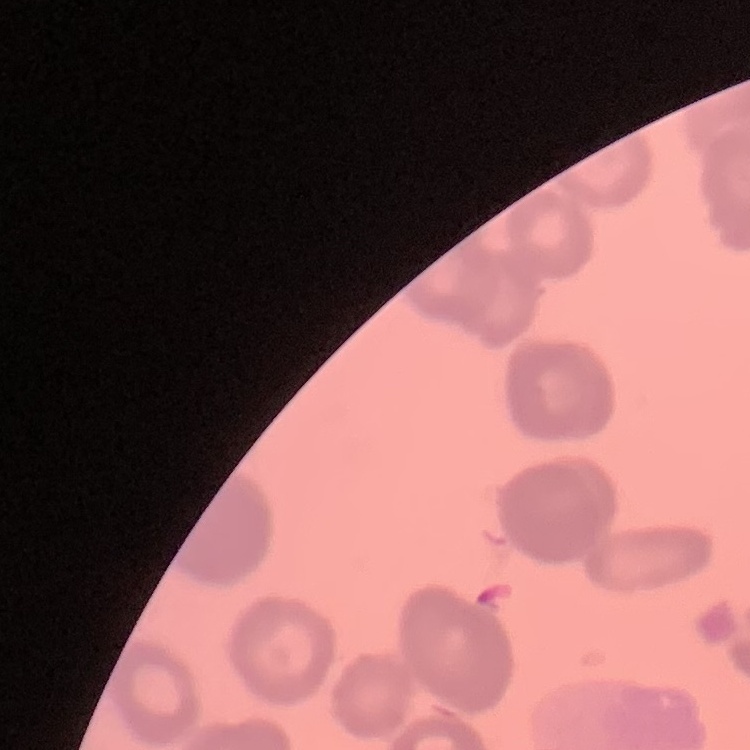

Summary:
  - Erythrocyte morphology: rouleaux formation
  - Preparation: thin blood smear
  - Image type: square crop of a larger photomicrograph
  - Stain: Field's or Giemsa